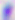

modality: micrograph
magnification: 400x
identification: Toxoplasma gondii